Assess the morphology of the red blood cells.
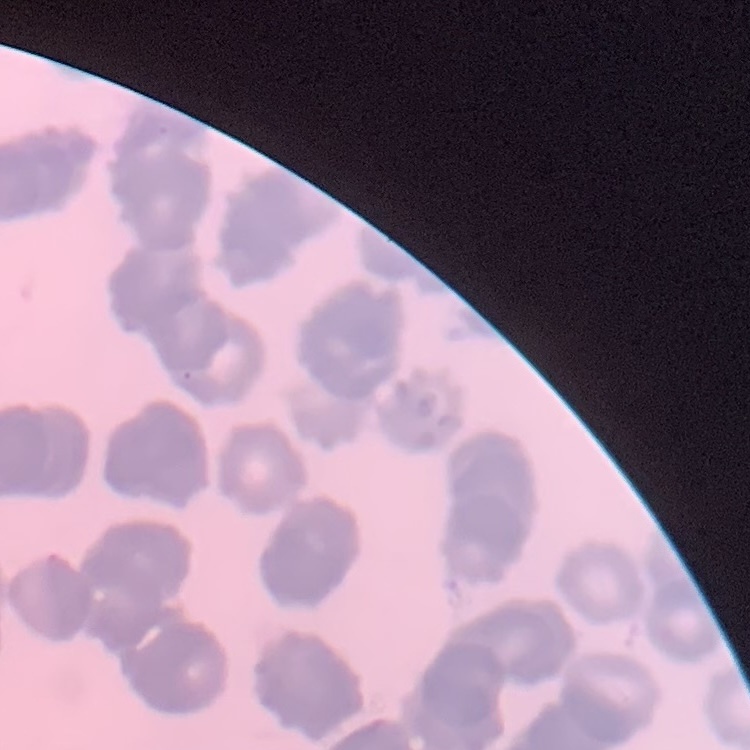

They show rouleaux formation.

Summary:
  - Stain: Field's or Giemsa
  - Image type: square crop of a larger photomicrograph
  - Preparation: thin blood smear